Report the malaria status of this cell.
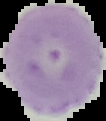

Uninfected.

Summary:
  - Image size: 106×121 pixels
  - Preparation: thin blood smear
  - Image type: cell region segmented out of the field of view; surrounding area masked to black